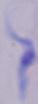
modality: photomicrograph
identification: trypanosome
magnification: 1000x